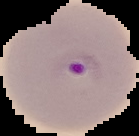
{
  "image_size": "139×136 pixels",
  "preparation": "thin blood smear",
  "malaria_status": "parasitized",
  "image_type": "segmented cell region on a black background"
}